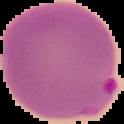

Summary:
  - Preparation: thin blood film
  - Result: malaria parasites identified
  - Image type: segmented cell region with the area outside set to black
  - Image size: 124×124 pixels